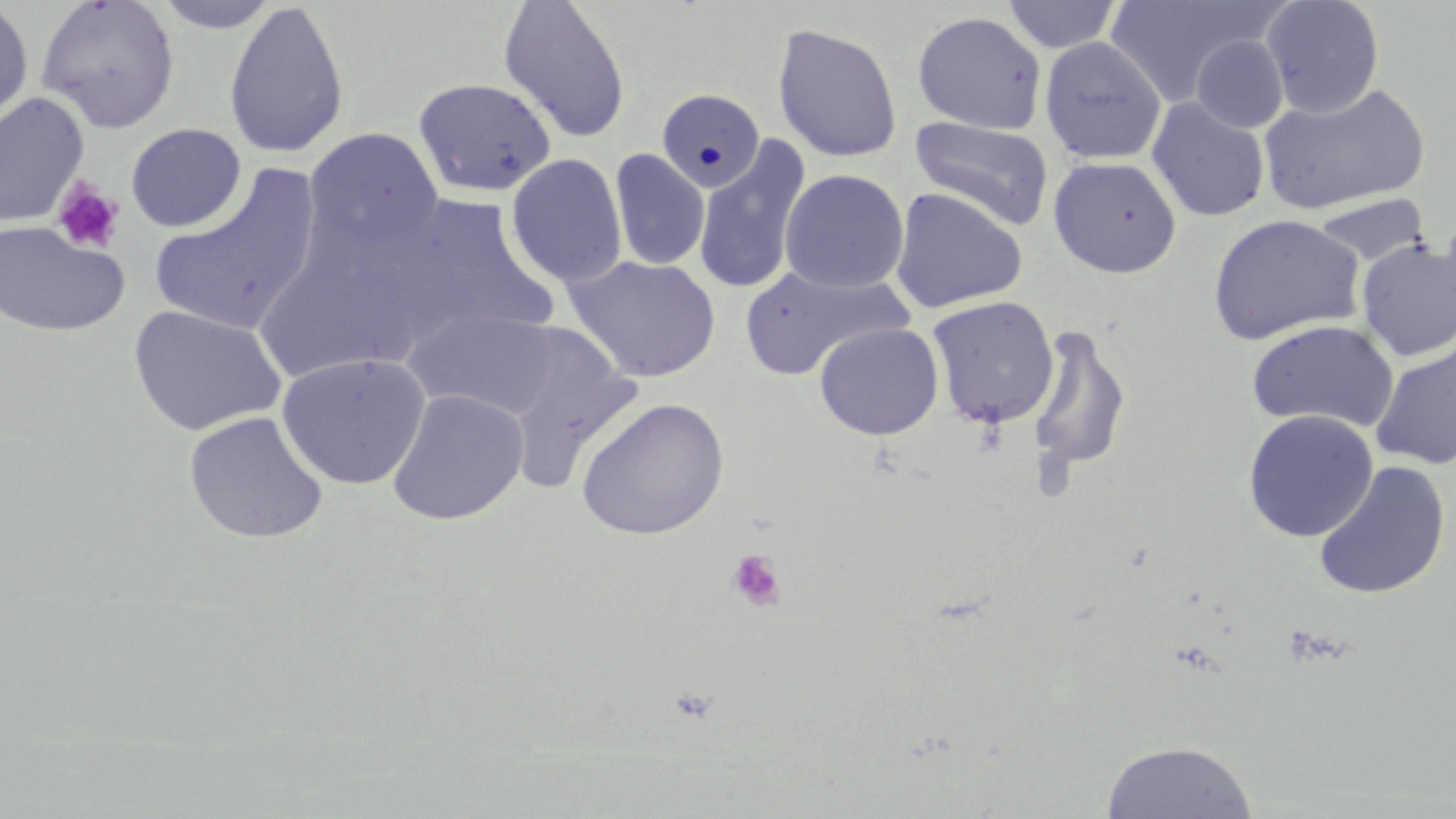

{
  "slide_level_diagnosis": "no evidence of blood parasites",
  "stain": "May-Grünwald-Giemsa",
  "image_size": "1456×819 pixels",
  "field_of_view": "one of a larger specimen",
  "uninfected_red_blood_cell_locations": "approximate bounding boxes as (x1, y1, x2, y2) in pixels: (35, 0, 180, 133), (498, 0, 631, 144), (1105, 0, 1275, 106), (1260, 0, 1385, 118), (0, 1, 35, 129), (154, 1, 280, 33), (224, 1, 349, 159), (1002, 1, 1121, 53), (912, 11, 1047, 134), (772, 22, 903, 164), (1191, 35, 1288, 134), (1040, 36, 1166, 164), (413, 76, 555, 198), (1258, 82, 1430, 216), (656, 88, 765, 193), (0, 92, 89, 229), (1147, 97, 1270, 223), (910, 116, 1055, 231), (125, 123, 247, 232), (304, 127, 444, 255), (693, 136, 811, 296), (609, 149, 709, 270), (506, 153, 628, 287), (1047, 156, 1182, 278), (150, 166, 323, 337), (779, 169, 909, 293), (889, 187, 1027, 314), (393, 194, 556, 343), (1312, 194, 1430, 266), (1207, 214, 1366, 346), (0, 221, 129, 338), (251, 238, 427, 386), (1356, 238, 1456, 362), (566, 255, 721, 383), (742, 264, 911, 380), (926, 296, 1060, 429), (128, 305, 287, 436), (404, 308, 561, 418), (1246, 320, 1400, 433), (814, 322, 944, 440), (1025, 324, 1131, 475), (503, 337, 642, 495), (1370, 340, 1456, 471), (276, 352, 430, 491), (387, 388, 529, 525), (575, 397, 730, 540), (1242, 409, 1379, 542), (183, 411, 329, 544), (1312, 461, 1451, 599), (1101, 739, 1259, 818)",
  "modality": "optical microscopy",
  "platelet_locations": "approximate bounding boxes as (x1, y1, x2, y2) in pixels: (52, 178, 126, 255), (727, 550, 786, 612)",
  "preparation": "thin blood film",
  "magnification": "1000x"
}